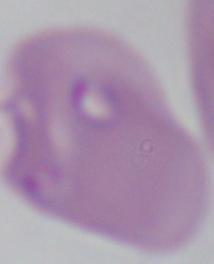

Summary:
  - Identification: Babesia
  - Modality: micrograph
  - Magnification: 1000x